Report the malaria status of this cell.
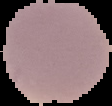

It is parasitized.

preparation: thin blood smear
image_type: segmented cell region with the area outside set to black
image_size: 112×106 pixels